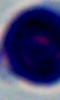
A white blood cell is shown. Photomicrograph. Captured at 1000x magnification.